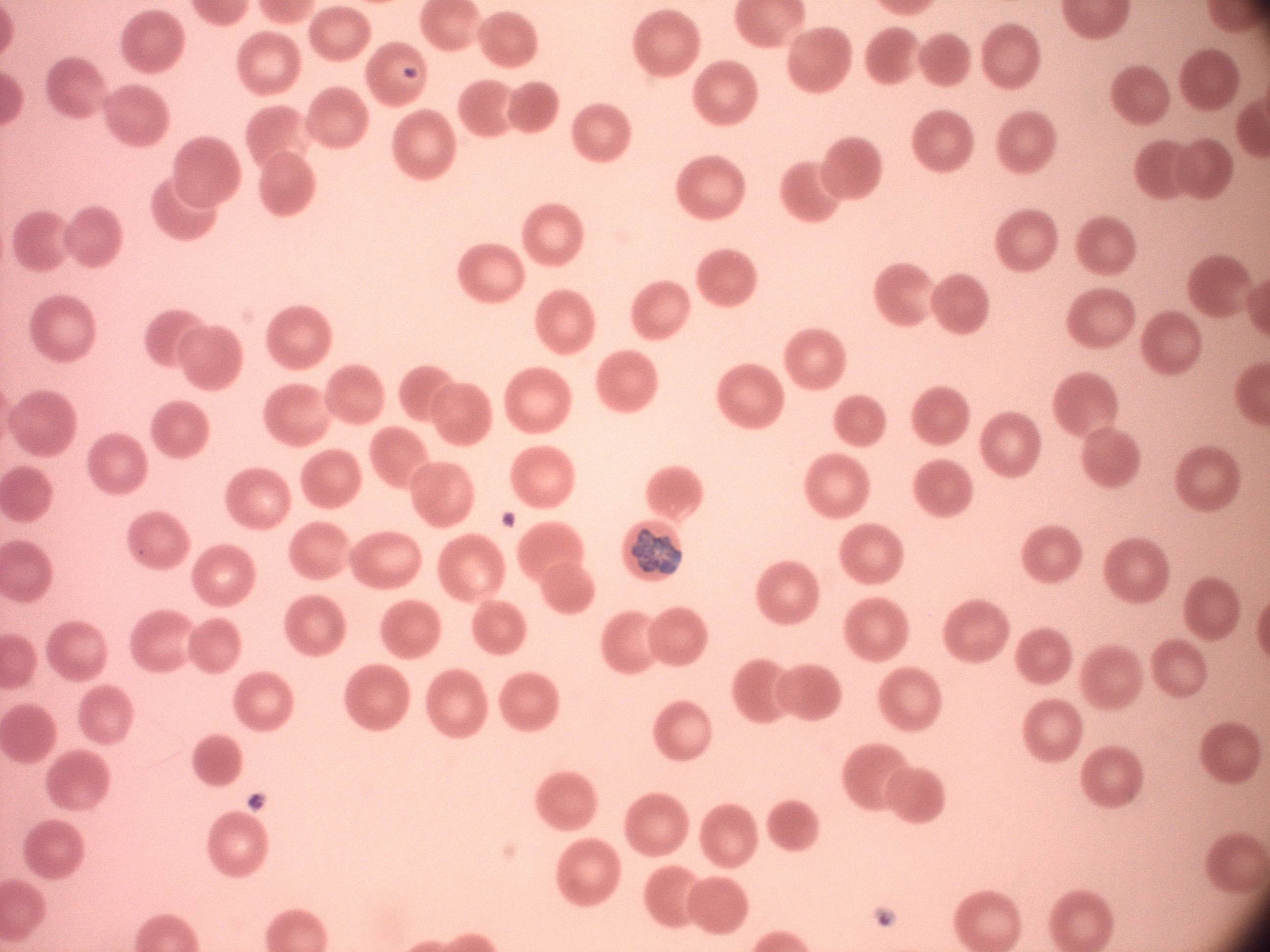
Approximate bounding boxes as (x1, y1, x2, y2) in pixels, from the source annotation, which is not necessarily exhaustive. Schizont locations: (631, 528, 683, 575). Image is 1270×952 pixels. One field from this slide. Giemsa stain. Thin blood film. Species: Plasmodium malariae. Acquired with a Leica DM2000 optical microscope and its built-in camera. 100x magnification.